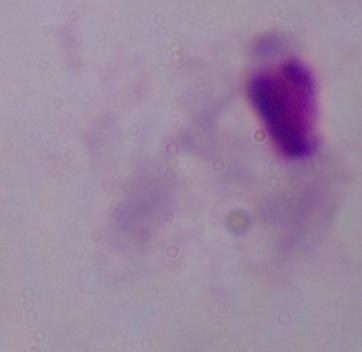

magnification: 1000x
modality: photomicrograph
identification: trichomonad